Name the blood parasite species.
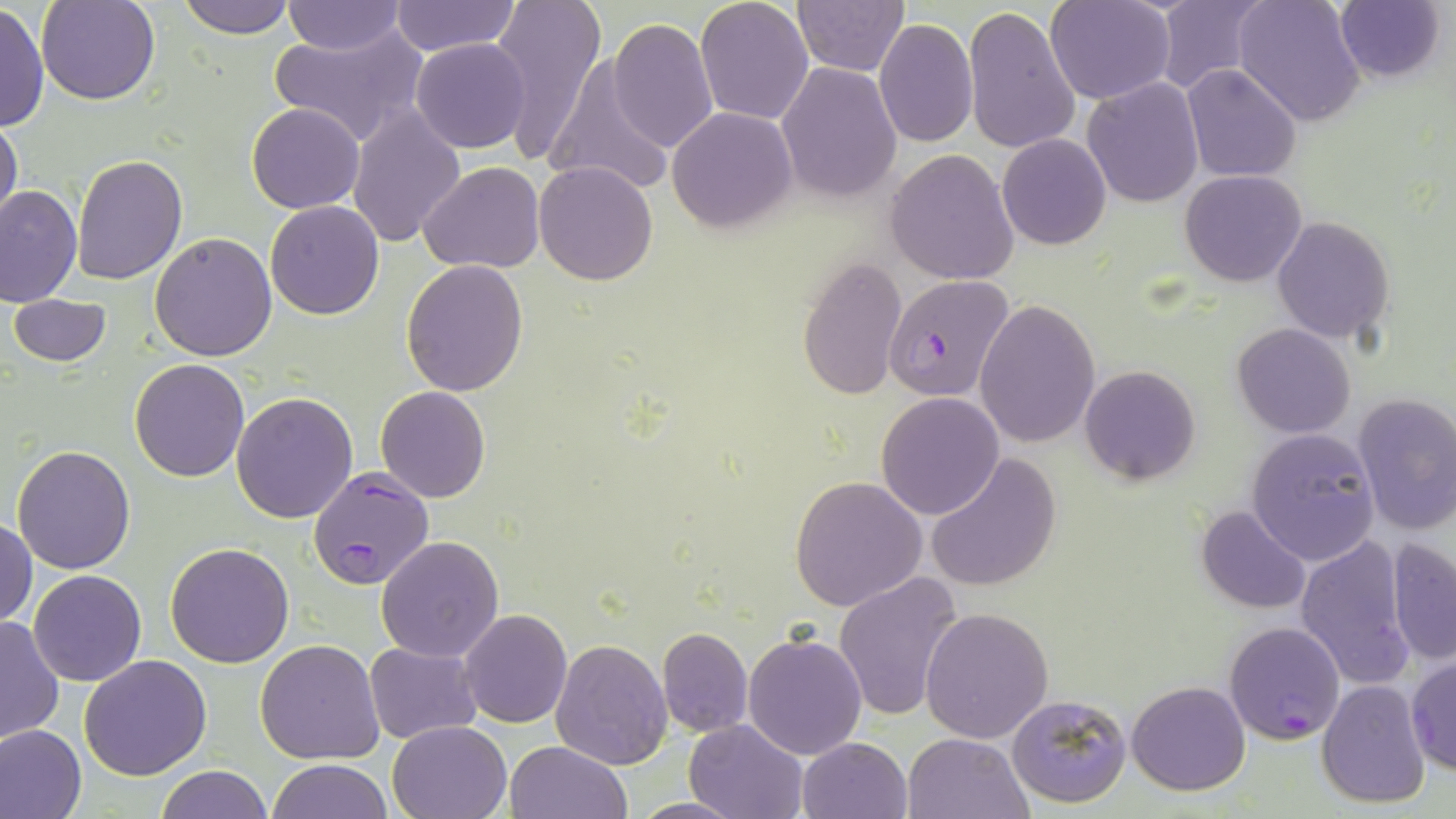

Plasmodium falciparum.

Summary:
  - Coordinate format: approximate bounding boxes as named x1/y1/x2/y2 corners in pixels
  - Plasmodium falciparum-infected red blood cell locations: (x1=884, y1=274, x2=1017, y2=404), (x1=309, y1=467, x2=434, y2=590), (x1=1225, y1=621, x2=1345, y2=743)
  - Uninfected red blood cell locations: (x1=37, y1=0, x2=161, y2=106), (x1=178, y1=0, x2=294, y2=39), (x1=491, y1=0, x2=608, y2=164), (x1=696, y1=0, x2=814, y2=124), (x1=791, y1=0, x2=908, y2=76), (x1=1047, y1=0, x2=1175, y2=104), (x1=1152, y1=0, x2=1269, y2=93), (x1=1233, y1=0, x2=1367, y2=126), (x1=389, y1=1, x2=521, y2=57), (x1=280, y1=2, x2=408, y2=55), (x1=1333, y1=2, x2=1446, y2=83), (x1=0, y1=3, x2=48, y2=133), (x1=962, y1=5, x2=1080, y2=157), (x1=875, y1=17, x2=978, y2=147), (x1=608, y1=19, x2=718, y2=155), (x1=268, y1=22, x2=426, y2=149), (x1=411, y1=39, x2=530, y2=154), (x1=542, y1=59, x2=674, y2=196), (x1=777, y1=61, x2=901, y2=203), (x1=1182, y1=64, x2=1302, y2=183), (x1=1083, y1=77, x2=1203, y2=208), (x1=246, y1=101, x2=365, y2=214), (x1=666, y1=105, x2=797, y2=235), (x1=348, y1=106, x2=466, y2=248), (x1=1, y1=115, x2=22, y2=231), (x1=996, y1=133, x2=1111, y2=250), (x1=886, y1=148, x2=1020, y2=284), (x1=73, y1=153, x2=188, y2=285), (x1=533, y1=161, x2=658, y2=285), (x1=419, y1=163, x2=544, y2=273), (x1=1181, y1=170, x2=1307, y2=287), (x1=1, y1=185, x2=82, y2=308), (x1=265, y1=200, x2=384, y2=320), (x1=1271, y1=216, x2=1395, y2=343), (x1=150, y1=232, x2=277, y2=360), (x1=796, y1=255, x2=907, y2=403), (x1=401, y1=258, x2=530, y2=396), (x1=9, y1=294, x2=111, y2=367), (x1=975, y1=299, x2=1100, y2=448), (x1=1232, y1=323, x2=1357, y2=439), (x1=129, y1=358, x2=250, y2=482), (x1=1078, y1=365, x2=1201, y2=484), (x1=375, y1=385, x2=490, y2=502), (x1=231, y1=391, x2=359, y2=523), (x1=1351, y1=392, x2=1456, y2=535), (x1=875, y1=393, x2=1005, y2=520), (x1=1246, y1=428, x2=1382, y2=565), (x1=11, y1=444, x2=137, y2=574), (x1=924, y1=452, x2=1061, y2=592), (x1=790, y1=475, x2=929, y2=612), (x1=1194, y1=505, x2=1311, y2=614), (x1=0, y1=518, x2=37, y2=630), (x1=376, y1=535, x2=504, y2=662), (x1=1295, y1=535, x2=1418, y2=692), (x1=1385, y1=538, x2=1455, y2=666), (x1=165, y1=543, x2=294, y2=666), (x1=27, y1=569, x2=146, y2=686), (x1=835, y1=572, x2=967, y2=722), (x1=921, y1=606, x2=1053, y2=743), (x1=459, y1=610, x2=572, y2=729), (x1=0, y1=616, x2=64, y2=746), (x1=657, y1=626, x2=752, y2=738), (x1=742, y1=631, x2=868, y2=760), (x1=551, y1=638, x2=672, y2=770), (x1=255, y1=639, x2=384, y2=765), (x1=365, y1=641, x2=484, y2=746), (x1=1406, y1=653, x2=1455, y2=775), (x1=79, y1=655, x2=211, y2=780), (x1=1318, y1=679, x2=1430, y2=808), (x1=1126, y1=680, x2=1250, y2=796), (x1=1007, y1=692, x2=1131, y2=808), (x1=685, y1=718, x2=806, y2=819), (x1=387, y1=719, x2=513, y2=818), (x1=0, y1=723, x2=87, y2=819), (x1=902, y1=731, x2=1031, y2=818), (x1=797, y1=736, x2=911, y2=819), (x1=506, y1=740, x2=631, y2=819), (x1=268, y1=760, x2=392, y2=818), (x1=157, y1=765, x2=272, y2=819), (x1=626, y1=796, x2=750, y2=818)
  - Field of view: single
  - Magnification: 1000x
  - Preparation: thin blood smear
  - Stain: May-Grünwald-Giemsa
  - Modality: optical microscopy
  - Image size: 1456×819 pixels